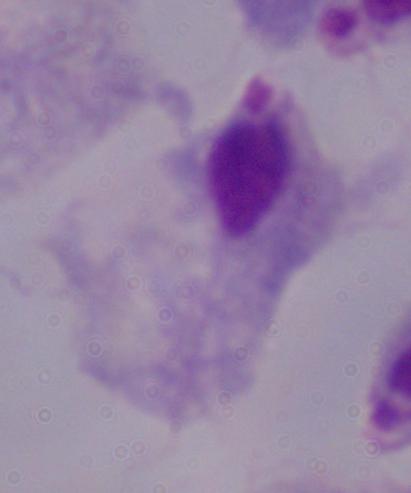

modality = micrograph
magnification = 1000x
identification = trichomonad